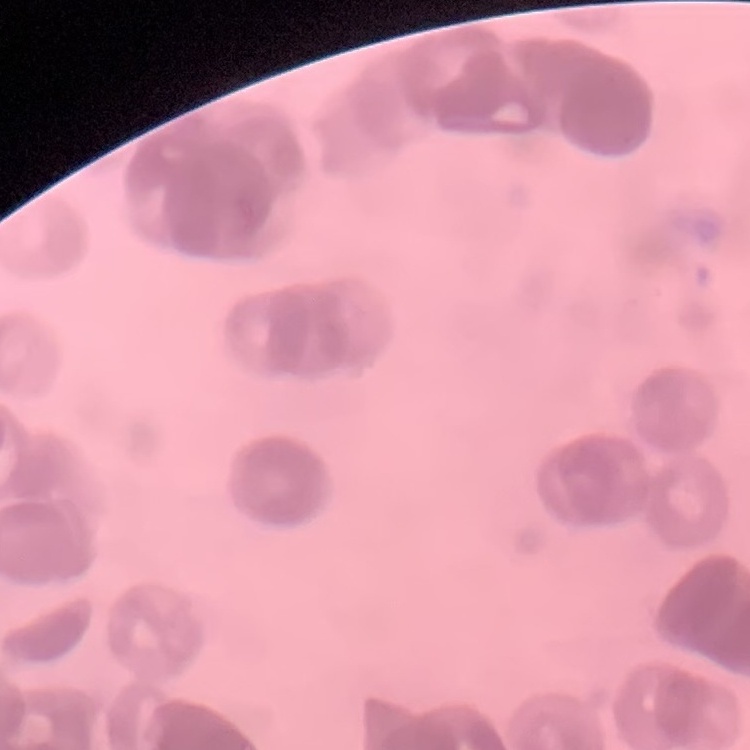 The erythrocytes exhibit rouleaux formation. Field's or Giemsa stain. One tile cut from a larger photomicrograph. Thin blood smear.